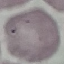

Summary:
  - Result: no malaria parasites seen
  - Capture: smartphone camera at the microscope eyepiece
  - Preparation: thin smear
  - Image type: automatically extracted cell patch, resized to 64 × 64 pixels
  - Stain: Giemsa